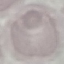
malaria status = uninfected
capture = smartphone camera at the microscope eyepiece
preparation = thin smear
image type = automatically extracted cell patch, resized to 64 × 64 pixels
stain = Giemsa